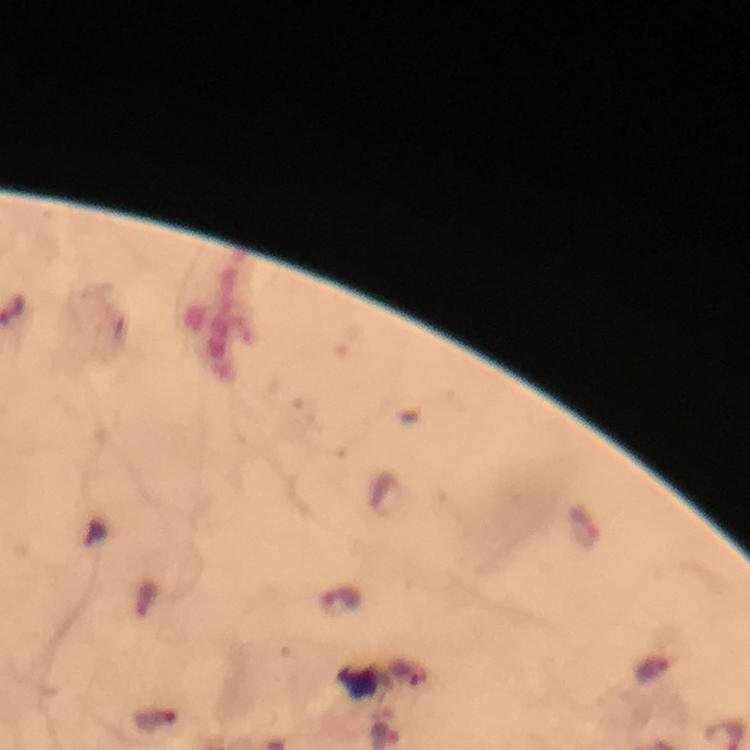 Approximate object centers, in pixels from the top-left corner. Plasmodium parasite locations: (x=342, y=602). A crop from one field of view. From a malaria diagnostic workup. Giemsa stain. Thick blood film. Image is 750×750 pixels. 100x magnification. Photographed through the microscope with a smartphone camera. Immersion oil was used.